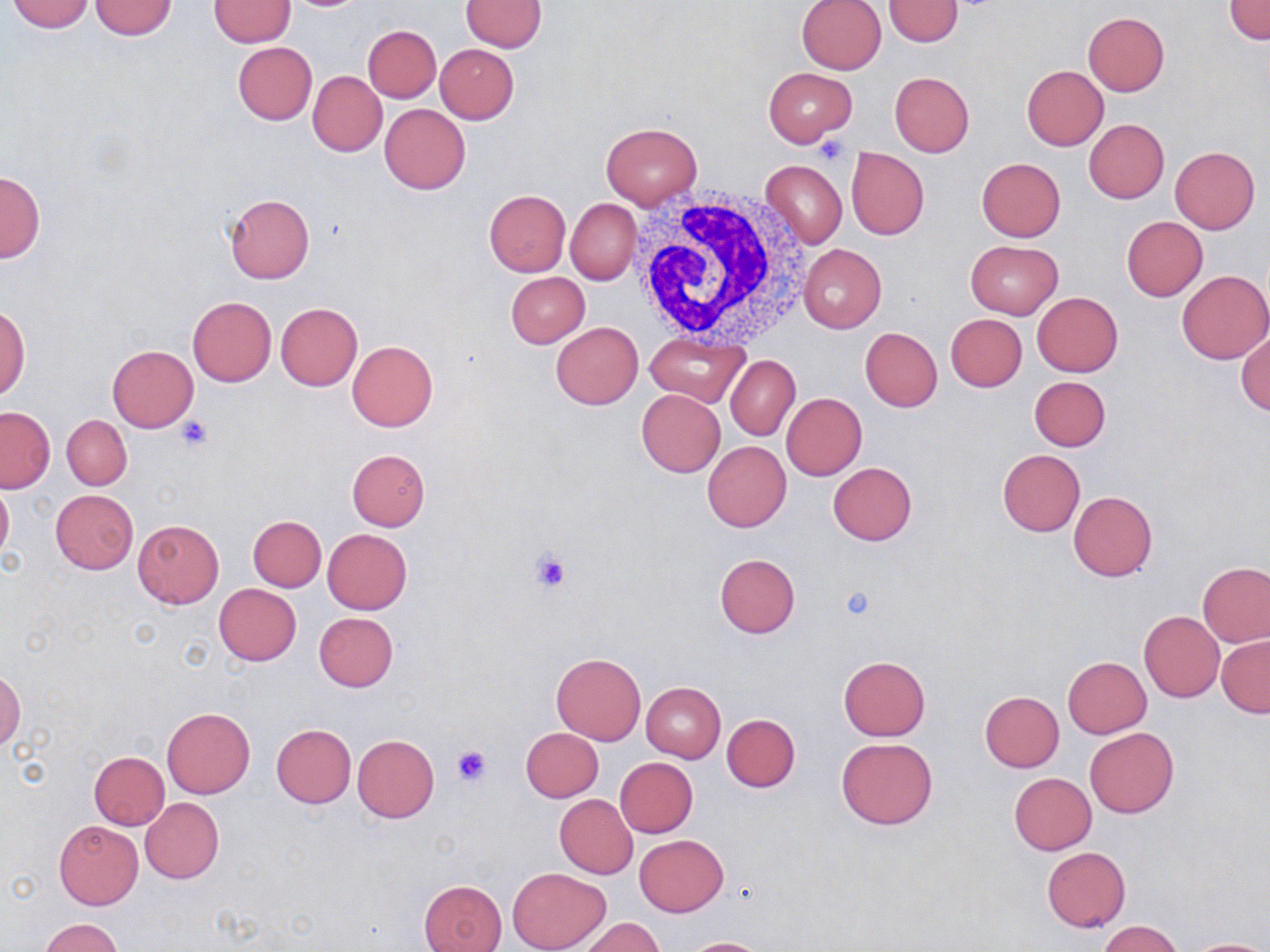
Approximate bounding boxes as named x1/y1/x2/y2 corners in pixels. Uninfected red blood cell locations: (x1=89, y1=0, x2=179, y2=41), (x1=882, y1=0, x2=965, y2=46), (x1=1226, y1=0, x2=1270, y2=43), (x1=4, y1=1, x2=95, y2=33), (x1=208, y1=1, x2=294, y2=47), (x1=461, y1=1, x2=546, y2=51), (x1=796, y1=1, x2=887, y2=74), (x1=1083, y1=12, x2=1169, y2=96), (x1=362, y1=25, x2=441, y2=101), (x1=232, y1=41, x2=315, y2=125), (x1=435, y1=44, x2=519, y2=124), (x1=1022, y1=65, x2=1109, y2=150), (x1=764, y1=68, x2=857, y2=147), (x1=308, y1=72, x2=386, y2=156), (x1=890, y1=72, x2=975, y2=157), (x1=380, y1=104, x2=470, y2=194), (x1=1084, y1=119, x2=1169, y2=203), (x1=601, y1=122, x2=702, y2=209), (x1=1170, y1=147, x2=1260, y2=234), (x1=845, y1=148, x2=928, y2=240), (x1=976, y1=158, x2=1065, y2=241), (x1=760, y1=159, x2=847, y2=248), (x1=0, y1=170, x2=45, y2=262), (x1=484, y1=190, x2=570, y2=276), (x1=225, y1=194, x2=315, y2=283), (x1=566, y1=199, x2=640, y2=285), (x1=1122, y1=216, x2=1207, y2=301), (x1=964, y1=240, x2=1063, y2=318), (x1=799, y1=243, x2=887, y2=332), (x1=505, y1=271, x2=589, y2=348), (x1=1178, y1=271, x2=1270, y2=364), (x1=1033, y1=292, x2=1123, y2=376), (x1=188, y1=296, x2=276, y2=386), (x1=276, y1=303, x2=362, y2=390), (x1=0, y1=308, x2=29, y2=400), (x1=946, y1=313, x2=1026, y2=391), (x1=551, y1=322, x2=644, y2=410), (x1=861, y1=327, x2=942, y2=411), (x1=1236, y1=328, x2=1270, y2=415), (x1=645, y1=335, x2=750, y2=408), (x1=347, y1=340, x2=438, y2=431), (x1=107, y1=345, x2=198, y2=431), (x1=726, y1=355, x2=799, y2=441), (x1=1029, y1=375, x2=1111, y2=450), (x1=637, y1=389, x2=725, y2=476), (x1=781, y1=392, x2=867, y2=481), (x1=0, y1=406, x2=55, y2=493), (x1=62, y1=415, x2=132, y2=490), (x1=702, y1=441, x2=792, y2=532), (x1=346, y1=449, x2=430, y2=530), (x1=998, y1=450, x2=1085, y2=536), (x1=828, y1=462, x2=917, y2=545), (x1=0, y1=479, x2=13, y2=568), (x1=51, y1=489, x2=139, y2=574), (x1=1069, y1=491, x2=1158, y2=580), (x1=248, y1=515, x2=325, y2=591), (x1=132, y1=520, x2=224, y2=608), (x1=323, y1=529, x2=412, y2=613), (x1=715, y1=553, x2=800, y2=638), (x1=1199, y1=564, x2=1270, y2=646), (x1=214, y1=584, x2=300, y2=666), (x1=1139, y1=611, x2=1224, y2=701), (x1=313, y1=612, x2=398, y2=692), (x1=1217, y1=635, x2=1270, y2=717), (x1=551, y1=652, x2=646, y2=744), (x1=838, y1=656, x2=931, y2=739), (x1=1062, y1=656, x2=1151, y2=737), (x1=0, y1=668, x2=24, y2=752), (x1=642, y1=683, x2=725, y2=762), (x1=980, y1=691, x2=1063, y2=772), (x1=162, y1=707, x2=256, y2=799), (x1=721, y1=714, x2=800, y2=792), (x1=272, y1=724, x2=356, y2=807), (x1=521, y1=727, x2=603, y2=802), (x1=1085, y1=728, x2=1178, y2=818), (x1=353, y1=734, x2=439, y2=822), (x1=836, y1=737, x2=938, y2=830), (x1=89, y1=751, x2=170, y2=830), (x1=616, y1=757, x2=697, y2=837), (x1=1009, y1=773, x2=1095, y2=854), (x1=554, y1=795, x2=638, y2=878), (x1=140, y1=797, x2=224, y2=883), (x1=53, y1=819, x2=143, y2=910), (x1=634, y1=835, x2=729, y2=916), (x1=1041, y1=847, x2=1130, y2=932), (x1=507, y1=867, x2=611, y2=952), (x1=419, y1=880, x2=508, y2=952), (x1=580, y1=917, x2=662, y2=952), (x1=39, y1=919, x2=124, y2=951), (x1=1099, y1=921, x2=1184, y2=952), (x1=681, y1=937, x2=769, y2=951), (x1=1186, y1=938, x2=1269, y2=952). Platelet locations: (x1=813, y1=136, x2=851, y2=165), (x1=176, y1=415, x2=213, y2=452), (x1=528, y1=548, x2=572, y2=593), (x1=840, y1=585, x2=878, y2=621), (x1=451, y1=744, x2=493, y2=787). White blood cell locations: (x1=627, y1=187, x2=812, y2=348). Slide-level diagnosis: no evidence of blood parasites. Light microscopy. Thin blood film. May-Grünwald-Giemsa stain. 1000x magnification. One field of a larger specimen. Image is 1270×952 pixels.